Assess for malaria.
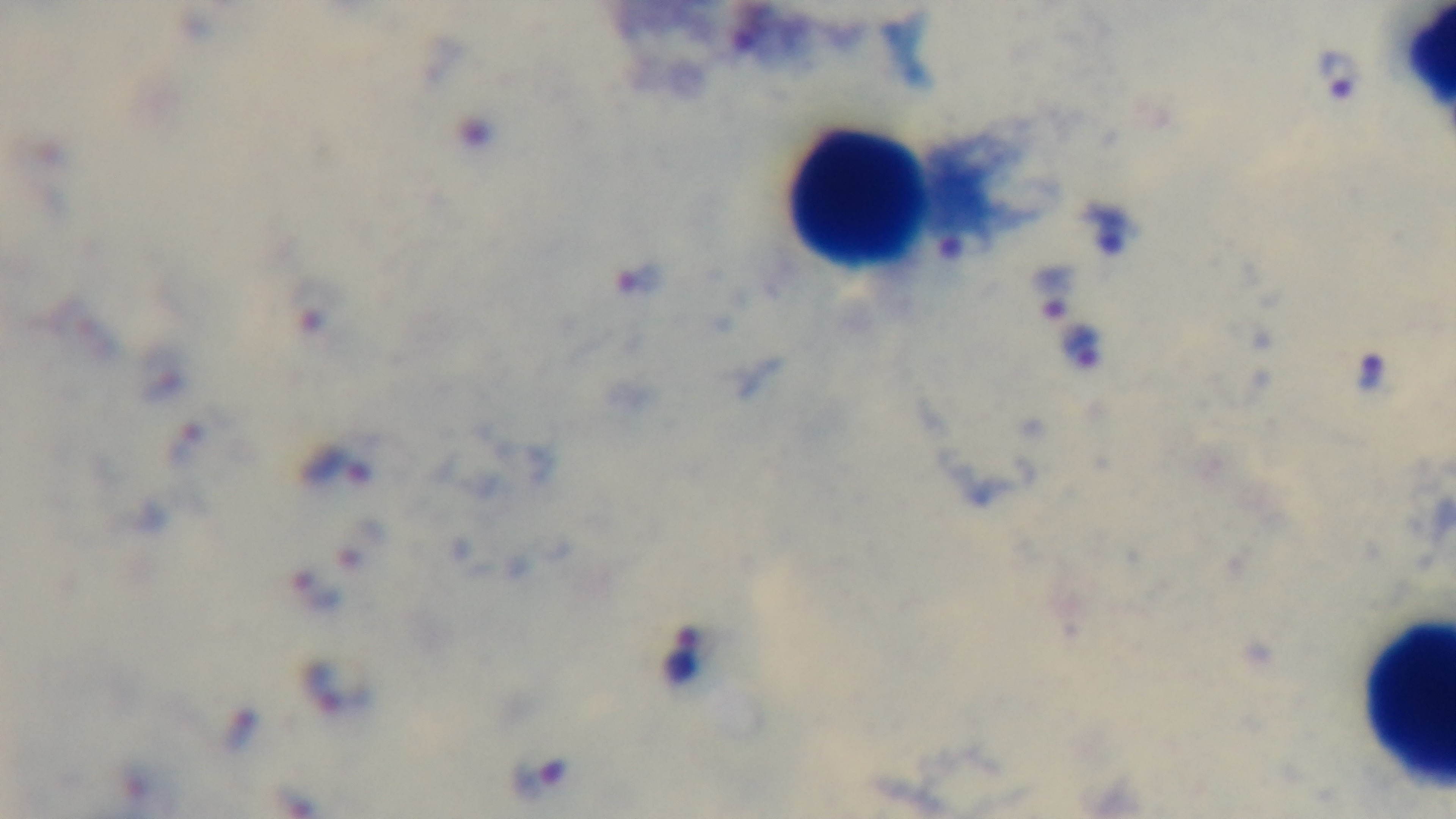
Positive.

Summary:
  - Modality: light microscopy
  - Preparation: thick
  - Capture: mounted 4K digital camera
  - Objective: 100x oil immersion
  - Field of view: one from the slide
  - Stain: Giemsa